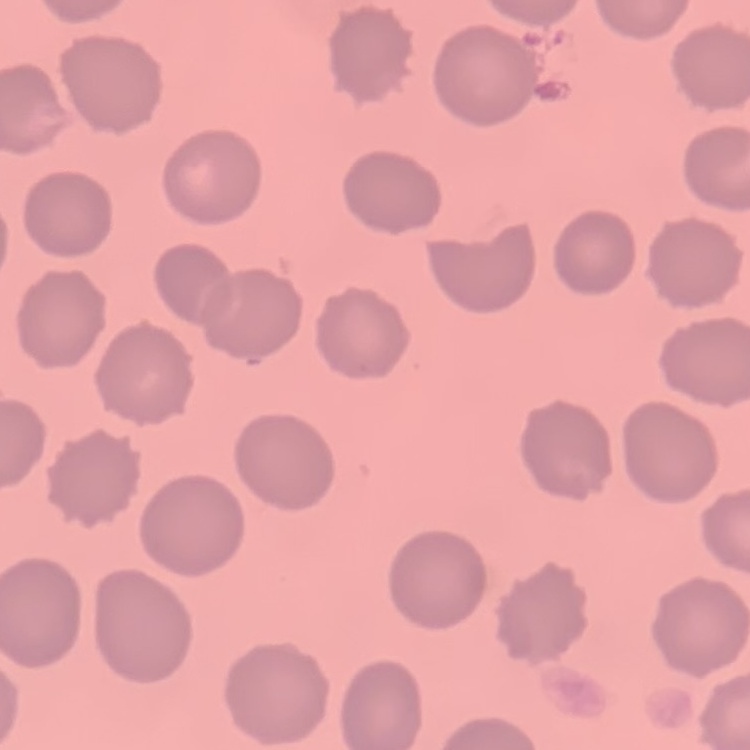

Summary:
  - Red blood cell morphology: no rouleaux formation
  - Stain: Field's or Giemsa
  - Preparation: thin blood film
  - Image type: one tile cut from a larger photomicrograph